Name the parasite shown.
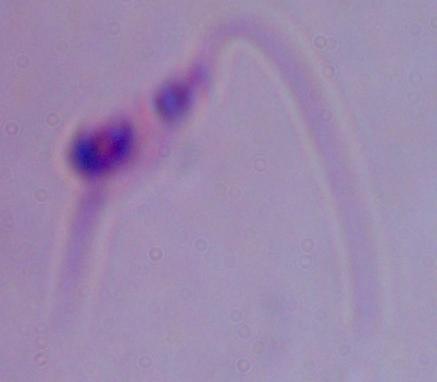

Leishmania.

Micrograph. 1000x magnification.